Point out each malaria parasite and each leukocyte.
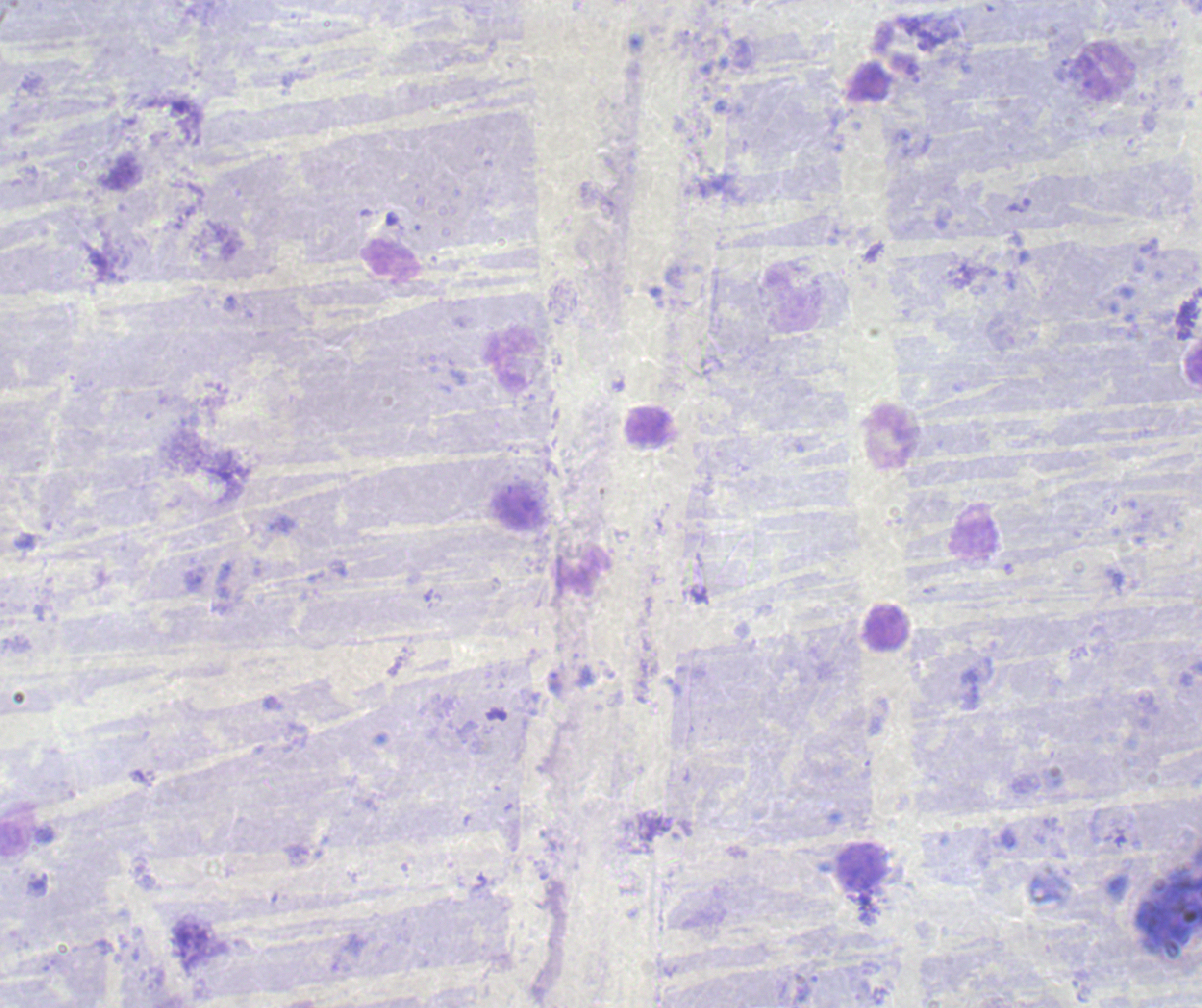

Negative for malaria parasites.
Approximate centers as {x, y} in pixels.
Leukocytes: {1105, 70}, {508, 360}, {647, 426}, {893, 437}, {582, 571}, {888, 631}, {860, 866}.

background quality = unsatisfactory
field of view = single
magnification = 100x
image size = 1202×1008 pixels
preparation = thick blood smear
stain = Romanowsky
context = previously used in a real diagnosis